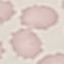
Summary:
  - Result: no malaria parasites detected
  - Image type: automatically extracted cell patch, resized to 64 × 64 pixels
  - Capture: smartphone camera at the microscope eyepiece
  - Stain: Giemsa
  - Preparation: thin smear